State which parasite is depicted.
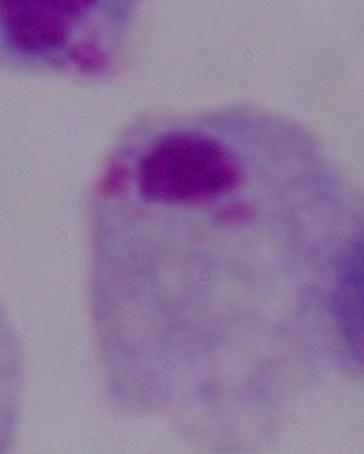

A trichomonad.

Micrograph. 1000x magnification.